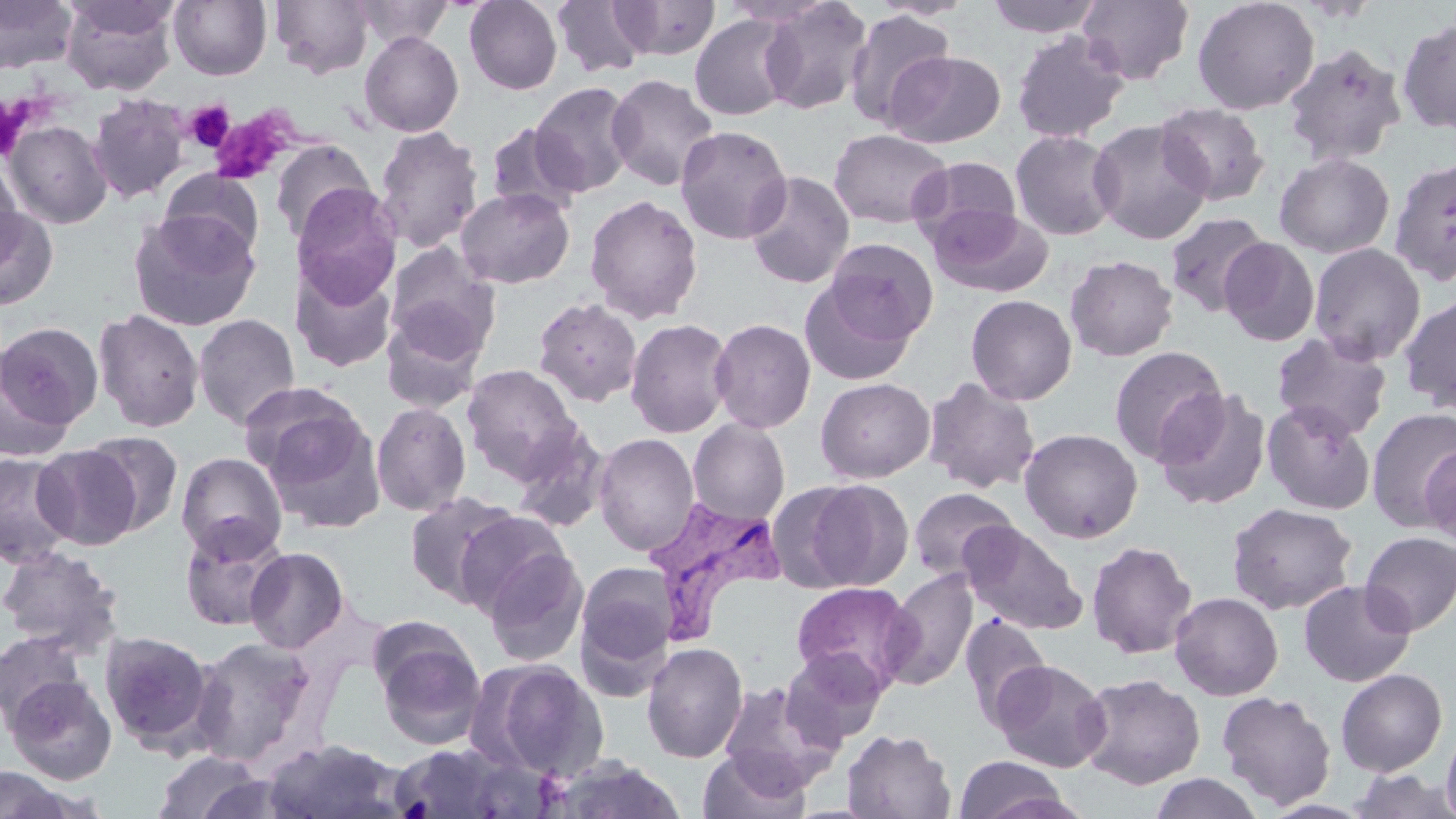

Summary:
  - Coordinate format: approximate bounding boxes as (x1, y1, x2, y2) in pixels
  - Uninfected red blood cell locations: (0, 0, 78, 74), (60, 0, 178, 95), (64, 0, 181, 40), (169, 0, 271, 80), (270, 0, 374, 79), (352, 0, 456, 48), (868, 0, 976, 20), (985, 0, 1104, 38), (1076, 0, 1195, 85), (1192, 0, 1319, 115), (464, 1, 563, 95), (551, 1, 652, 78), (612, 1, 721, 60), (757, 1, 873, 115), (843, 9, 956, 130), (689, 14, 796, 120), (1397, 17, 1456, 135), (1011, 30, 1129, 143), (359, 31, 464, 137), (1282, 43, 1408, 167), (885, 50, 1007, 148), (606, 73, 720, 191), (529, 81, 638, 197), (88, 93, 191, 203), (1155, 102, 1270, 207), (1089, 118, 1213, 244), (4, 120, 112, 228), (486, 122, 583, 217), (374, 125, 484, 253), (674, 125, 792, 245), (828, 128, 951, 229), (1010, 129, 1121, 241), (270, 139, 375, 244), (1274, 152, 1395, 258), (911, 155, 1022, 248), (1389, 157, 1456, 286), (0, 160, 24, 271), (158, 169, 265, 264), (744, 170, 855, 289), (292, 185, 401, 306), (455, 187, 574, 289), (584, 194, 703, 324), (928, 204, 1052, 297), (0, 208, 58, 309), (129, 211, 261, 332), (1164, 212, 1271, 316), (1220, 237, 1320, 347), (824, 238, 938, 344), (385, 243, 500, 363), (1309, 243, 1426, 365), (1066, 255, 1179, 361), (292, 265, 396, 372), (799, 280, 917, 385), (1399, 293, 1456, 415), (966, 294, 1077, 405), (532, 297, 643, 407), (94, 308, 205, 433), (381, 312, 486, 411), (193, 314, 300, 431), (625, 317, 734, 438), (709, 318, 816, 433), (0, 322, 103, 432), (1271, 332, 1393, 440), (1109, 345, 1229, 466), (0, 347, 72, 463), (462, 364, 582, 482), (815, 377, 935, 483), (923, 377, 1040, 494), (240, 383, 365, 481), (1154, 388, 1272, 510), (1262, 400, 1377, 515), (371, 402, 471, 516), (1367, 408, 1456, 530), (262, 410, 384, 534), (688, 419, 790, 524), (510, 424, 611, 532), (1019, 428, 1143, 543), (82, 431, 184, 536), (593, 433, 699, 555), (1421, 444, 1456, 547), (33, 445, 142, 550), (0, 451, 77, 569), (177, 452, 286, 560), (797, 479, 913, 591), (908, 487, 1019, 582), (404, 491, 521, 607), (1226, 502, 1358, 615), (453, 510, 570, 617), (179, 517, 289, 631), (961, 520, 1089, 635), (1359, 531, 1456, 636), (1086, 540, 1197, 659), (1084, 542, 1200, 790), (0, 545, 125, 657), (481, 546, 588, 666), (244, 547, 349, 654), (575, 562, 678, 676), (882, 569, 978, 691), (1299, 579, 1415, 687), (791, 581, 918, 695), (1170, 592, 1283, 700), (959, 613, 1052, 729), (370, 622, 487, 749), (0, 631, 87, 727), (99, 631, 215, 751), (190, 637, 317, 766), (641, 642, 748, 763), (781, 647, 887, 746), (474, 658, 610, 781), (991, 659, 1111, 772), (647, 668, 809, 783), (1335, 668, 1447, 777), (1077, 673, 1206, 789), (5, 674, 116, 785), (717, 679, 843, 795), (1217, 690, 1336, 809), (1441, 724, 1456, 819), (842, 729, 956, 818), (263, 739, 409, 818), (387, 741, 543, 818), (698, 747, 812, 819), (152, 751, 268, 819), (953, 755, 1072, 819), (542, 756, 689, 819), (0, 767, 79, 818), (1348, 767, 1455, 818), (1149, 772, 1263, 818), (1260, 799, 1375, 819)
  - Platelet locations: (184, 101, 234, 151), (220, 112, 296, 183)
  - Plasmodium vivax-infected red blood cell locations: (644, 497, 786, 643)
  - Slide-level diagnosis: Plasmodium vivax
  - Stain: May-Grünwald-Giemsa
  - Image size: 1456×819 pixels
  - Modality: light microscopy
  - Field of view: single
  - Preparation: thin blood smear
  - Magnification: 1000x